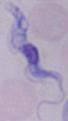

magnification = 1000x
modality = micrograph
identification = trypanosome